Identify the parasite.
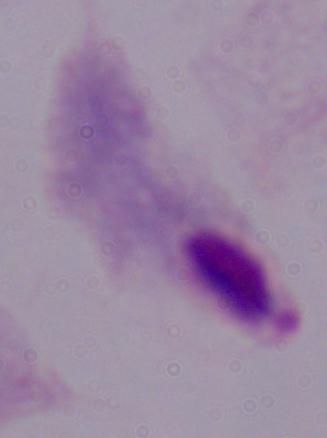

This is a trichomonad.

Summary:
  - Magnification: 1000x
  - Modality: micrograph